Give the position of every malaria parasite.
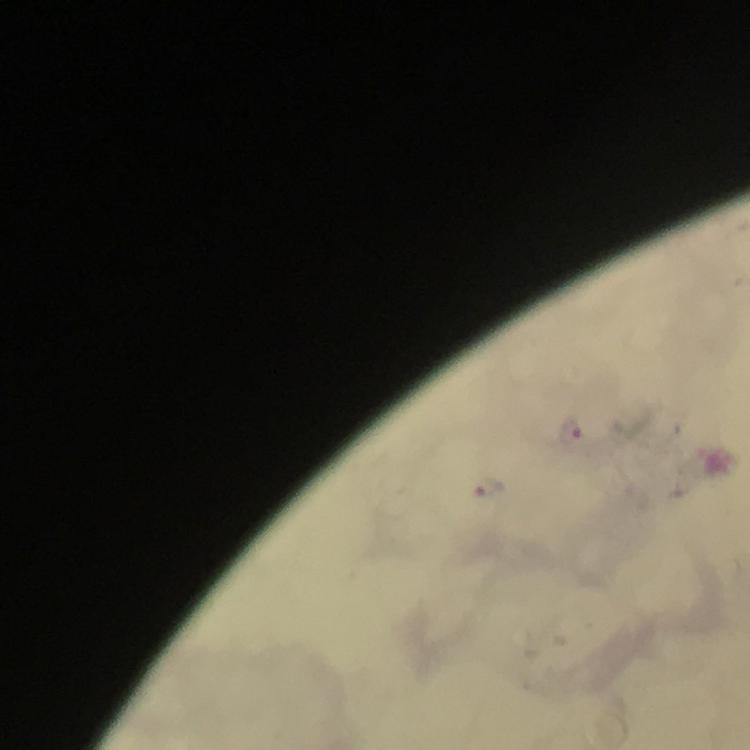
Approximate centers as [x, y] in pixels.
Malaria parasites: [570, 428], [490, 484].

Thick smear. 100x magnification. Cropped region of a single field of view. Photographed with a smartphone mounted on the microscope. From a diagnostic examination for malaria. Image is 750×750 pixels. Immersion oil applied. Giemsa-stained preparation.